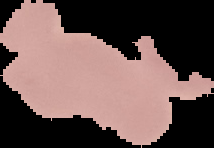
Malaria status: uninfected. Segmented cell region on a black background. Image is 214×148 pixels. From a thin blood film.